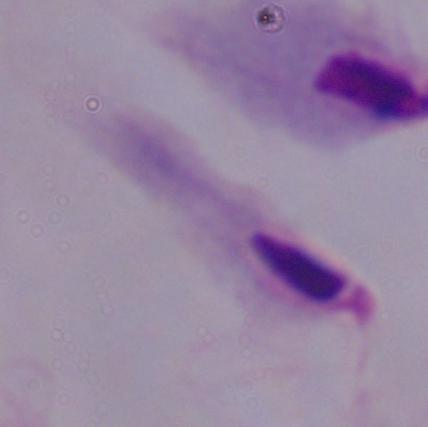

identification = trichomonad
modality = micrograph
magnification = 1000x